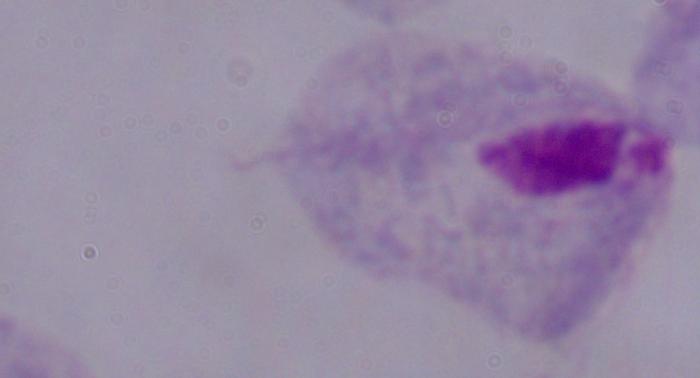

Summary:
  - Modality: micrograph
  - Magnification: 1000x
  - Identification: trichomonad